Draw a bounding box around every trophozoite.
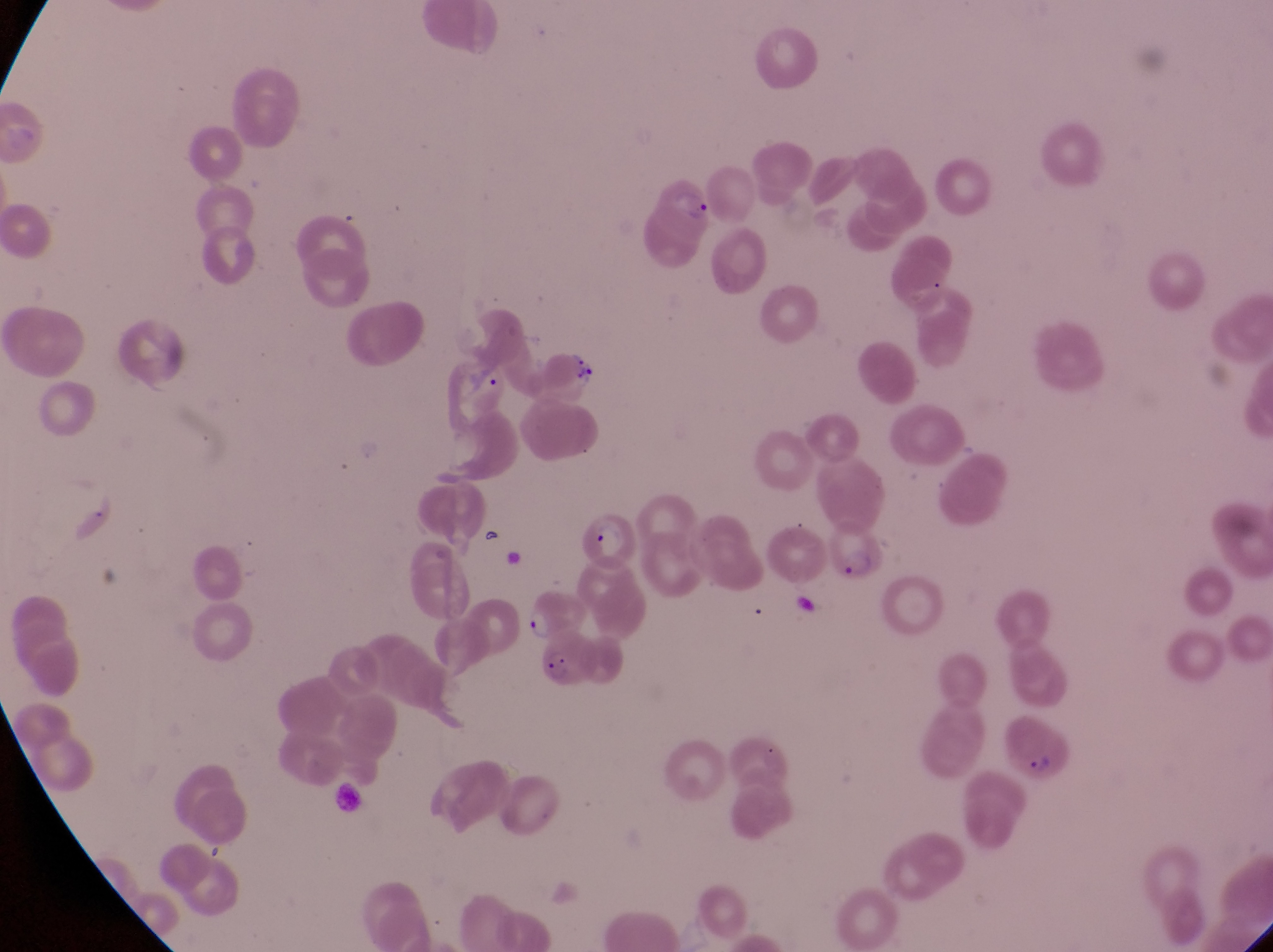

Approximate bounding boxes as {left, top, right, bottom} in pixels.
Trophozoites: {474, 364, 502, 396}, {529, 610, 552, 643}.

parasitised_red_blood_cell_locations: 'approximate bounding boxes as {left, top, right, bottom} in pixels: {634, 162, 717, 266}, {569, 502, 638, 565}, {828, 515, 883, 583}, {541, 631, 611, 691}, {1008, 711, 1080, 785}'
field_of_view: single
country: Uganda
preparation: thin blood film
image_size: 1273×952 pixels
artifact_platelet_like_body_stain_precipitate_or_debris_locations: 'approximate bounding boxes as {left, top, right, bottom} in pixels: {564, 347, 597, 386}'
magnification: 1000x
capture: smartphone photograph through the eyepiece of an Olympus CX-23 microscope